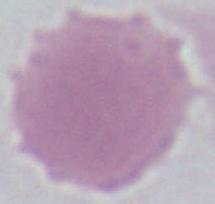

modality = photomicrograph
identification = red blood cell
magnification = 1000x